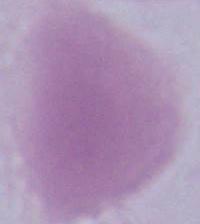
{
  "identification": "erythrocyte",
  "magnification": "1000x",
  "modality": "photomicrograph"
}